Assess this cell for malaria.
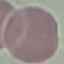
Uninfected.

Summary:
  - Stain: Giemsa
  - Capture: smartphone through the microscope eyepiece
  - Image type: automatically extracted cell patch, resized to 64 × 64 pixels
  - Preparation: thin blood smear